Identify the parasite.
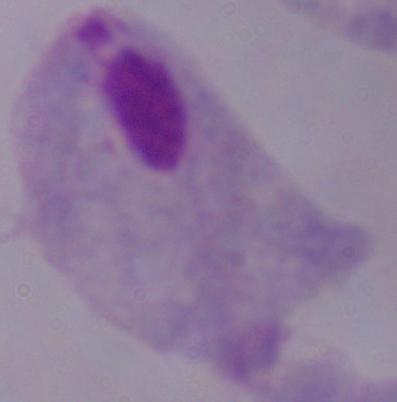

A trichomonad.

Photomicrograph. Captured at 1000x magnification.